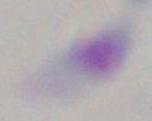

Micrograph. Toxoplasma gondii is seen. 1000x magnification.